Report the malaria status of this cell.
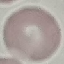

It is uninfected.

stain = Giemsa
preparation = thin blood film
image type = automatically extracted cell patch, resized to 64 × 64 pixels
capture = smartphone through the microscope eyepiece